Comment on the morphology of the red blood cells.
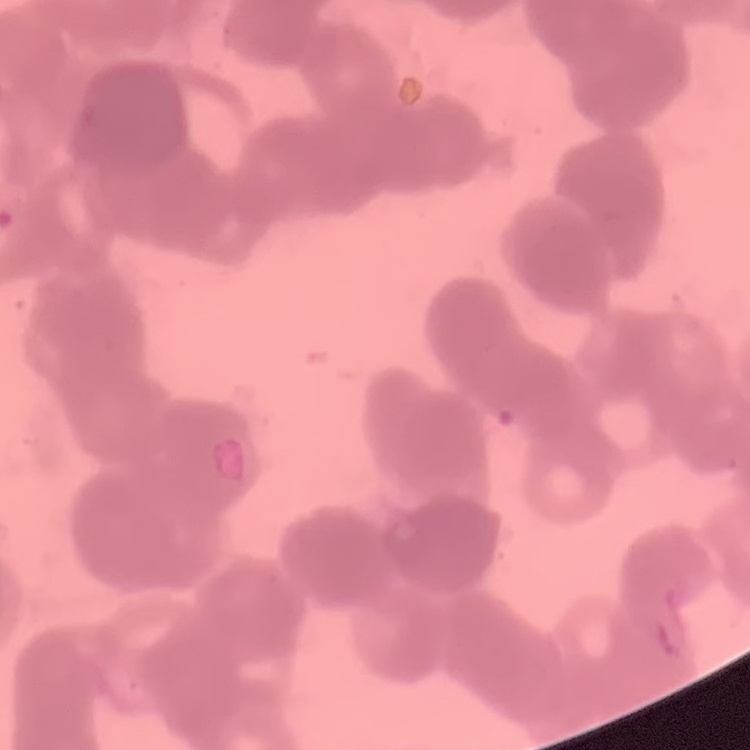
They show rouleaux formation.

Field's or Giemsa stain. Square crop of a larger photomicrograph. Thin peripheral smear.